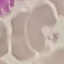
Result: no malaria parasites seen. Acquired by smartphone through the microscope eyepiece. Automatically extracted cell patch, resized to 64 × 64 pixels. Giemsa stain. Thin blood smear.